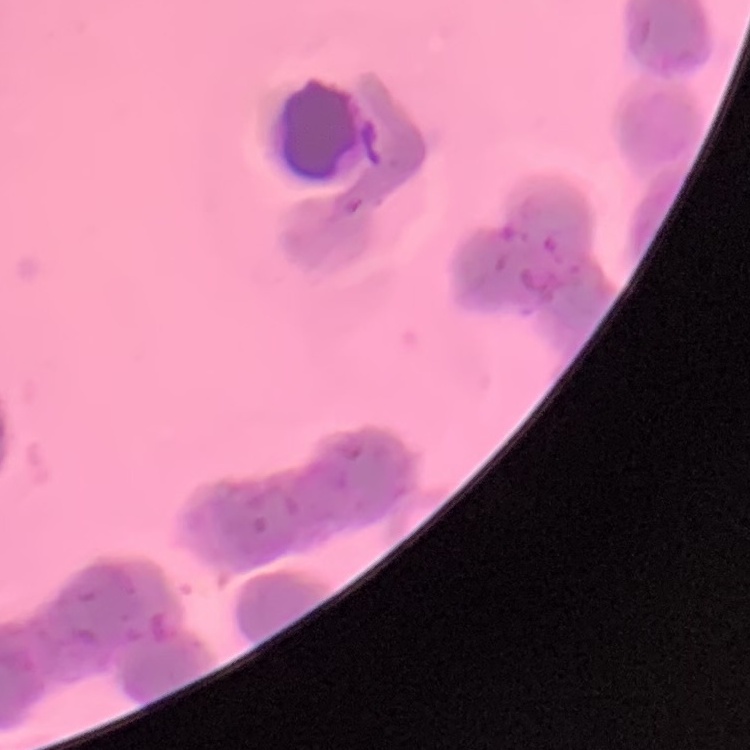
Summary:
  - Erythrocyte morphology: rouleaux formation
  - Stain: Field's or Giemsa
  - Preparation: thin blood smear
  - Image type: one tile cut from a larger photomicrograph